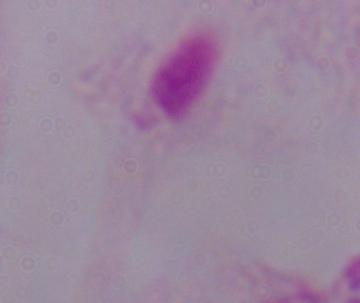
A trichomonad is shown. Captured at 1000x magnification. Photomicrograph.